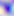
magnification = 400x
identification = Toxoplasma gondii
modality = micrograph